Classify this cell by malaria status.
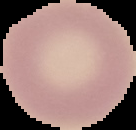

It is uninfected.

From a thin blood film. Image is 136×130 pixels. Cell region segmented out of the field of view; the surrounding area is masked to black.